State which parasite is depicted.
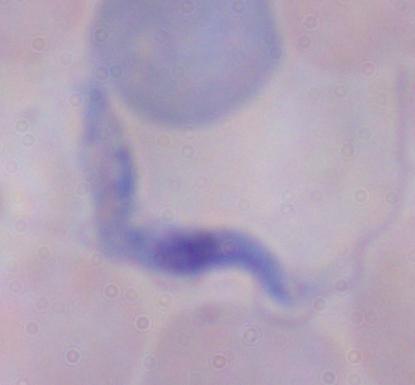

A trypanosome.

modality = photomicrograph
magnification = 1000x